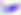

Captured at 400x magnification. Toxoplasma gondii is shown. Micrograph.